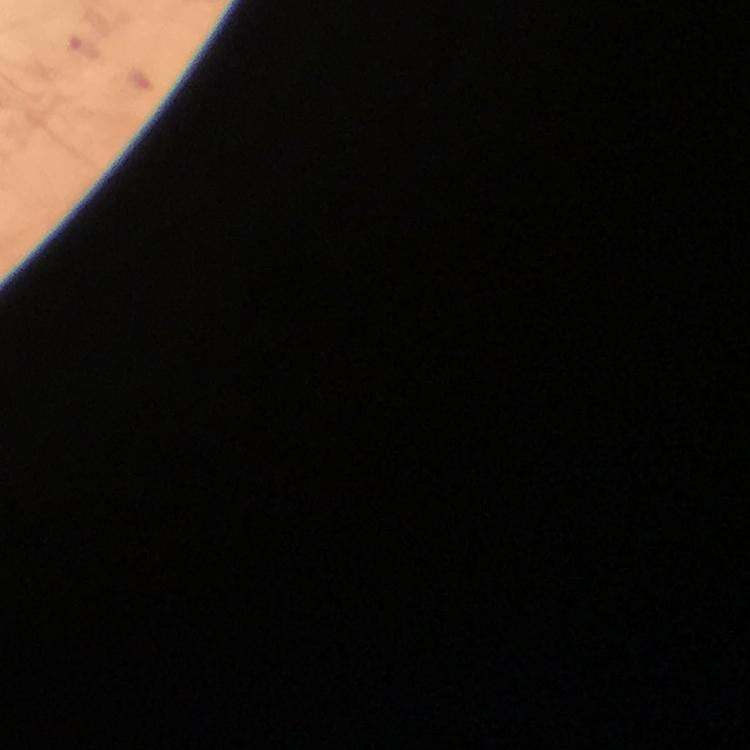
image_size: 750×750 pixels
immersion_oil: applied
context: from a diagnostic examination for malaria
preparation: thick blood smear
plasmodium_parasite_locations: 'approximate centers as (x, y) in pixels: (83, 47), (139, 81)'
stain: Giemsa
cropped_from: a single field of view
magnification: 100x
capture: smartphone mounted on the microscope